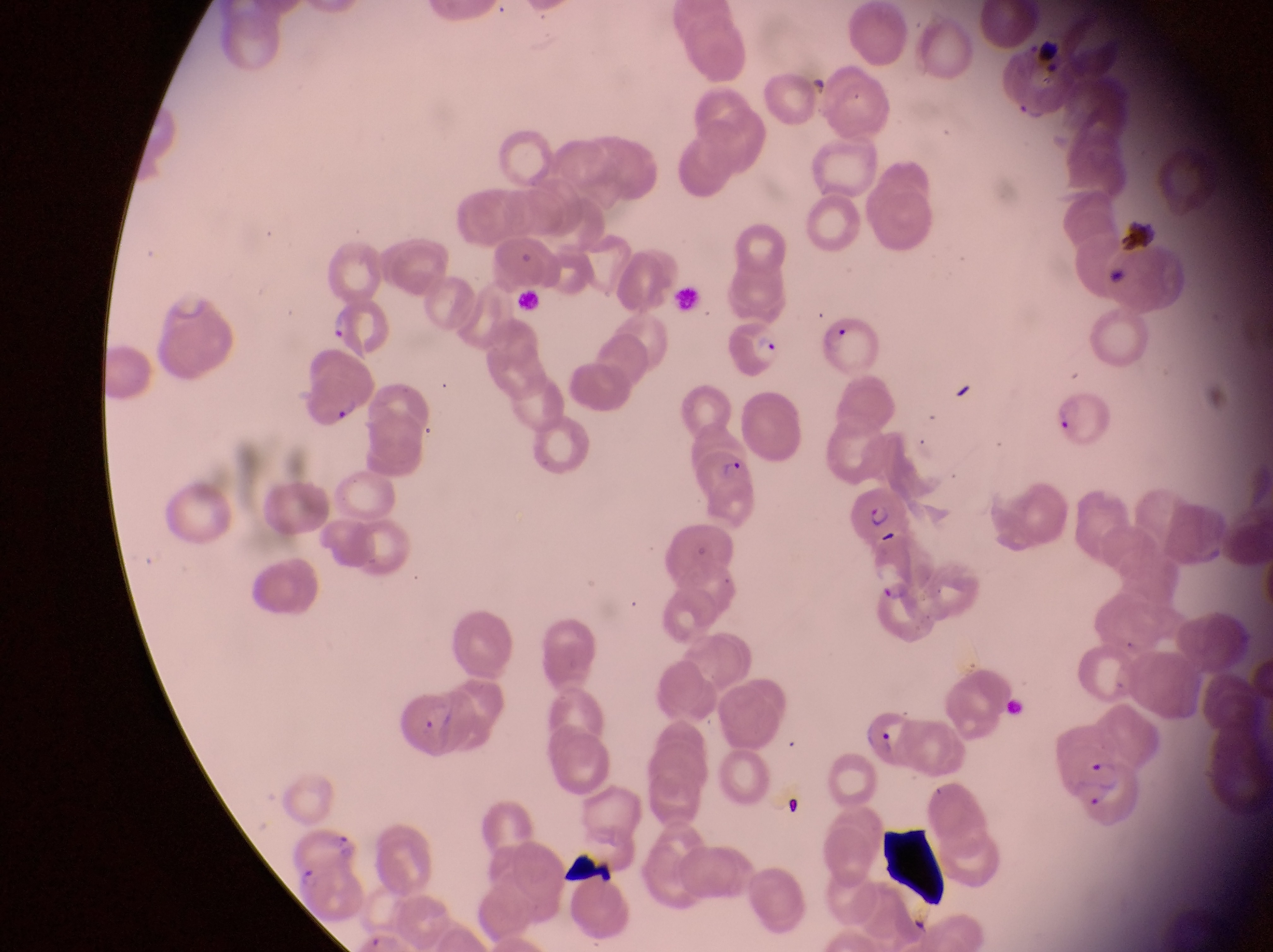

Approximate bounding boxes as [left, top, right, bottom] in pixels.
Summary:
  - Artifact (platelet-like body, stain precipitate, or debris) locations: [1121, 215, 1153, 253], [877, 824, 948, 910], [567, 851, 613, 892]
  - Parasitised red blood cell locations: [327, 307, 394, 360], [816, 313, 883, 373], [719, 317, 786, 380], [1056, 389, 1119, 452], [694, 447, 761, 524], [851, 480, 913, 548], [873, 580, 935, 647], [395, 687, 475, 765], [864, 705, 917, 767], [1078, 756, 1155, 836], [292, 864, 369, 927]
  - Country: Uganda
  - Magnification: 1000x
  - Image size: 1273×952 pixels
  - Field of view: single
  - Preparation: thin blood film
  - Capture: smartphone photograph through the eyepiece of an Olympus CX-23 microscope